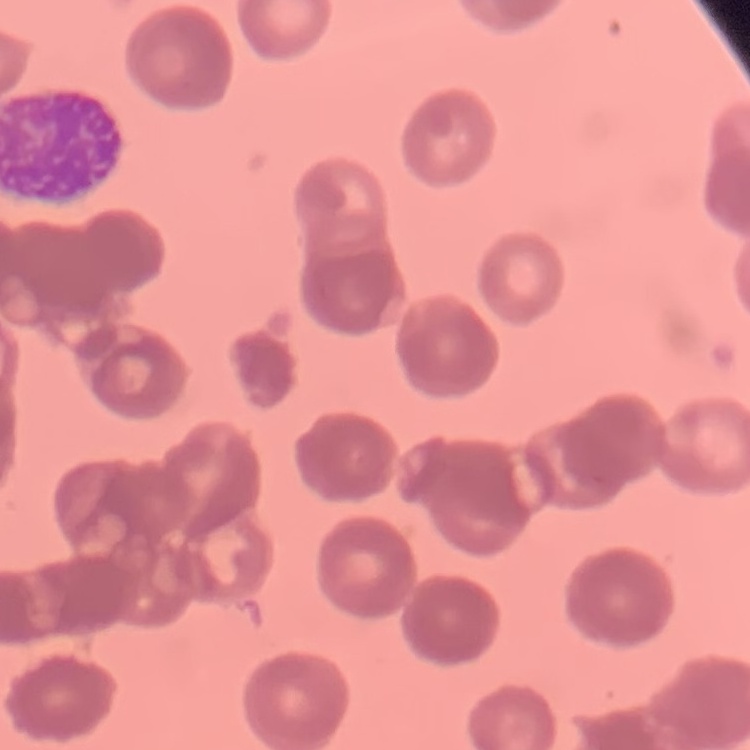
{
  "red_blood_cell_morphology": "rouleaux formation",
  "stain": "Field's or Giemsa",
  "image_type": "one tile cut from a larger photomicrograph",
  "preparation": "thin peripheral smear"
}